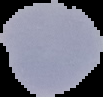

Summary:
  - Result: malaria parasites identified
  - Image type: segmented cell region on a black background
  - Image size: 103×97 pixels
  - Preparation: thin blood smear